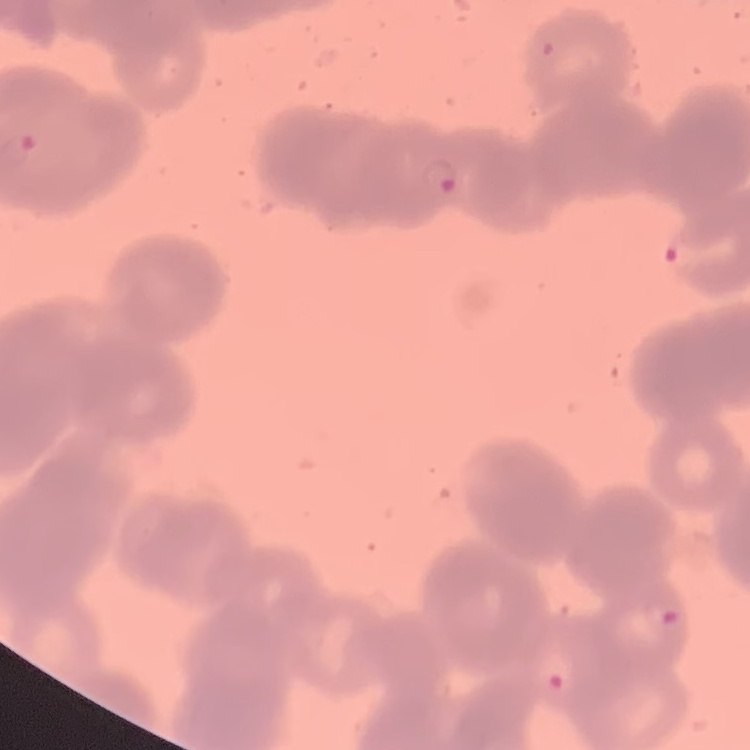
Summary:
  - Red blood cell morphology: rouleaux formation
  - Image type: one tile cut from a larger photomicrograph
  - Preparation: thin peripheral smear
  - Stain: Field's or Giemsa